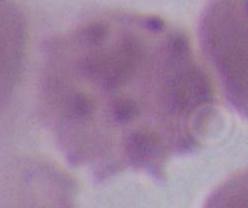
A red blood cell is seen. Photomicrograph. Captured at 1000x magnification.